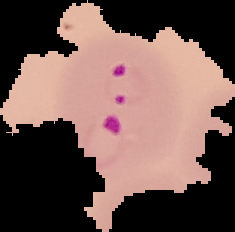 Result: Plasmodium parasites identified. The area outside the segmented cell region is set to black. Image is 235×232 pixels. From a thin blood film.